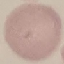 Result: no malaria parasites detected. Thin blood film. Automatically extracted cell patch, resized to 64 × 64 pixels. Acquired by smartphone through the microscope eyepiece. Giemsa stain.